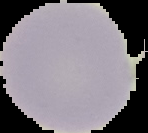
{
  "image_type": "cell region segmented out of the field of view; surrounding area masked to black",
  "result": "negative for malaria parasites",
  "preparation": "thin blood smear",
  "image_size": "148×133 pixels"
}